Assess this cell for malaria.
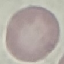
It is uninfected.

{
  "image_type": "automatically extracted cell patch, resized to 64 × 64 pixels",
  "preparation": "thin blood film",
  "stain": "Giemsa",
  "capture": "smartphone through the microscope eyepiece"
}